Classify this cell by malaria status.
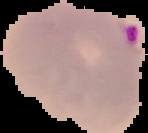

Parasitized.

image_size: 148×133 pixels
preparation: thin blood smear
image_type: segmented cell region with the area outside set to black